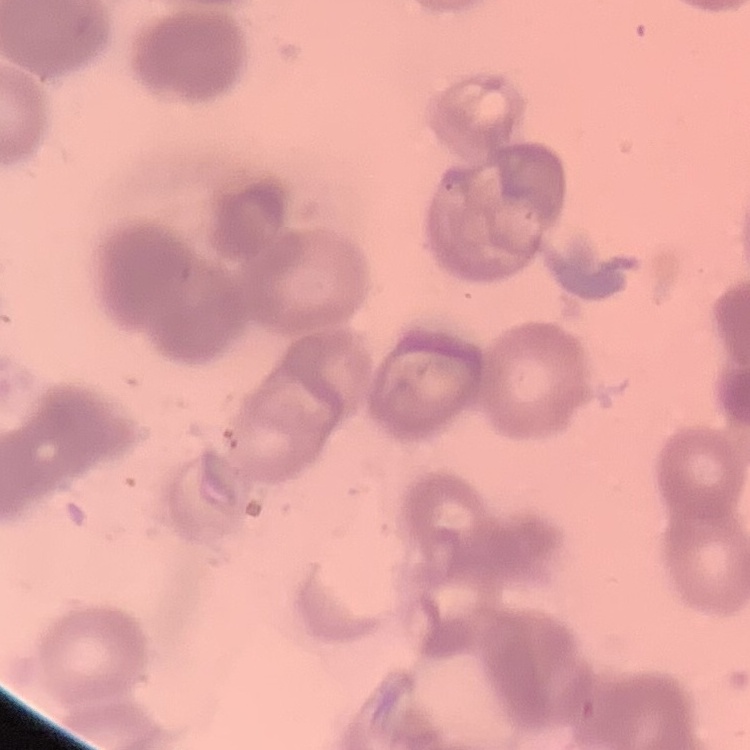

erythrocyte_morphology: rouleaux formation
image_type: one tile cut from a larger photomicrograph
preparation: thin blood film
stain: Field's or Giemsa